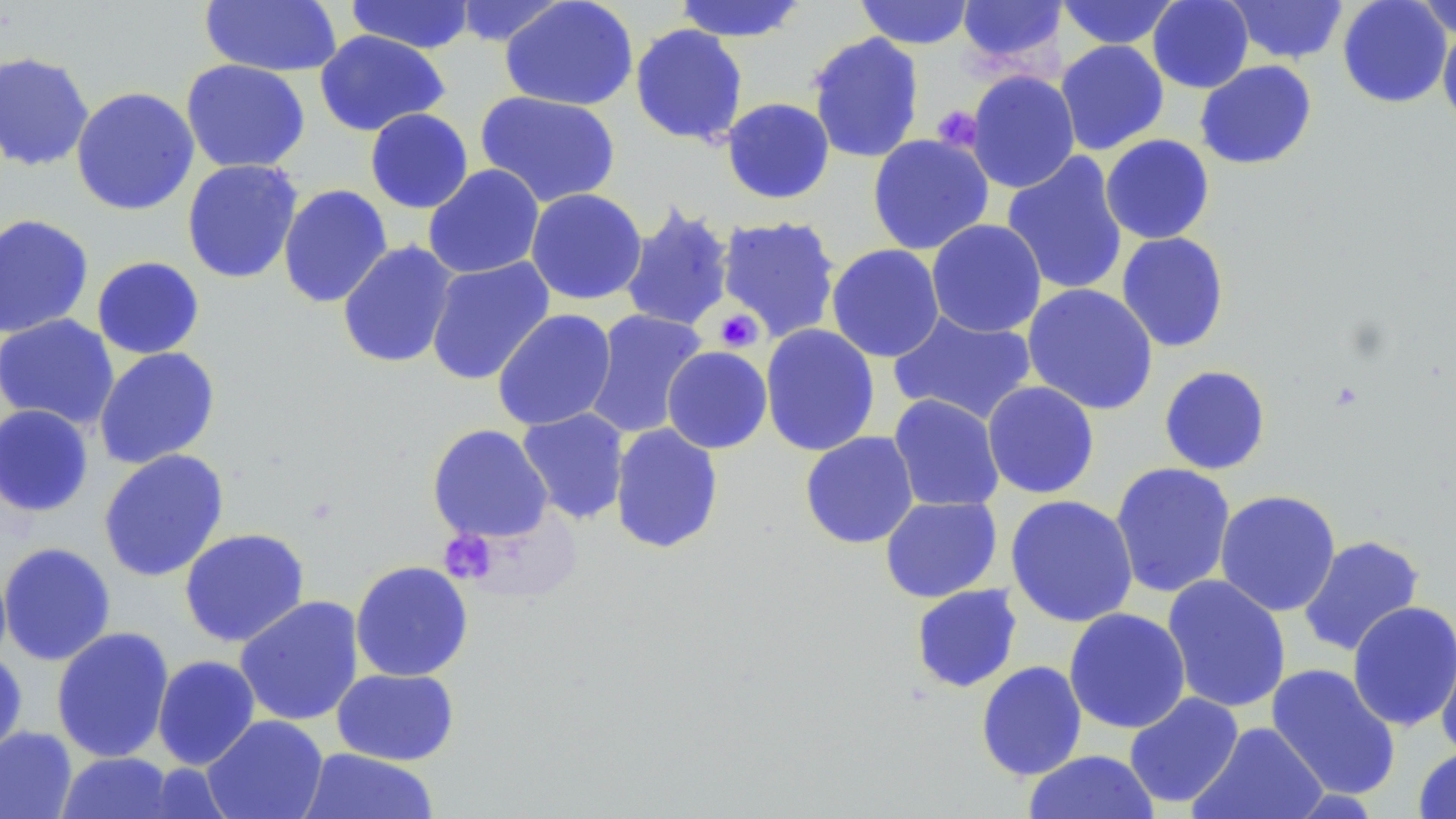

slide_level_diagnosis: no evidence of blood parasites
preparation: thin blood smear
magnification: 1000x
modality: light microscopy
platelet_locations: 'approximate bounding boxes as [x1, y1, x2, y2] in pixels: [932, 106, 981, 151], [714, 309, 763, 352], [439, 530, 497, 585]'
field_of_view: one of a larger specimen
uninfected_red_blood_cell_locations: 'approximate bounding boxes as [x1, y1, x2, y2] in pixels: [344, 0, 476, 54], [673, 0, 809, 42], [854, 0, 976, 49], [957, 0, 1066, 72], [1057, 0, 1181, 49], [1147, 0, 1254, 93], [1225, 0, 1349, 65], [1337, 0, 1453, 108], [1414, 0, 1456, 38], [199, 1, 342, 77], [449, 1, 569, 48], [499, 1, 639, 111], [629, 23, 749, 146], [1437, 24, 1456, 134], [314, 30, 450, 136], [806, 31, 925, 164], [1056, 39, 1169, 155], [0, 51, 94, 172], [180, 59, 310, 174], [1194, 60, 1317, 170], [965, 70, 1080, 193], [70, 86, 199, 216], [474, 90, 622, 208], [721, 97, 835, 204], [365, 108, 473, 214], [867, 133, 994, 255], [1100, 134, 1215, 244], [1001, 151, 1129, 296], [181, 159, 304, 284], [423, 164, 544, 279], [278, 184, 393, 308], [525, 188, 648, 305], [618, 202, 736, 334], [0, 213, 94, 338], [715, 215, 842, 342], [926, 219, 1047, 338], [1116, 232, 1230, 353], [336, 240, 459, 370], [826, 243, 945, 362], [91, 256, 205, 359], [425, 257, 555, 385], [1021, 283, 1158, 415], [492, 309, 617, 431], [584, 309, 709, 439], [888, 309, 1038, 426], [0, 314, 119, 430], [760, 323, 880, 457], [662, 346, 773, 454], [94, 347, 221, 469], [1159, 365, 1271, 475], [981, 381, 1100, 499], [887, 394, 1005, 513], [0, 404, 93, 518], [516, 408, 631, 525], [426, 423, 554, 543], [609, 423, 724, 555], [799, 431, 919, 549], [98, 449, 230, 582], [1110, 462, 1236, 599], [1215, 489, 1341, 617], [1005, 494, 1139, 628], [880, 496, 1002, 603], [179, 528, 310, 647], [1297, 534, 1426, 658], [0, 542, 116, 666], [0, 556, 12, 670], [350, 560, 474, 682], [1162, 574, 1291, 713], [909, 584, 1022, 693], [235, 595, 365, 726], [1346, 600, 1456, 732], [1063, 608, 1191, 734], [51, 626, 175, 763], [1435, 632, 1456, 764], [0, 647, 28, 762], [152, 654, 261, 770], [975, 660, 1087, 781], [1265, 663, 1401, 801], [331, 667, 459, 766], [1124, 691, 1244, 809], [202, 714, 329, 819], [1189, 722, 1328, 818], [0, 726, 77, 819], [1413, 746, 1456, 818], [298, 748, 439, 819], [1022, 749, 1159, 819], [56, 751, 179, 818]'
stain: May-Grünwald-Giemsa
image_size: 1456×819 pixels